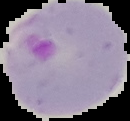
malaria status = parasitized
image size = 130×121 pixels
image type = segmented cell region on a black background
preparation = thin blood smear